Assess this cell for malaria.
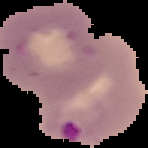
It is parasitized.

Image is 148×148 pixels. From a thin blood film. The area outside the segmented cell region is set to black.